Describe the morphology of the erythrocytes.
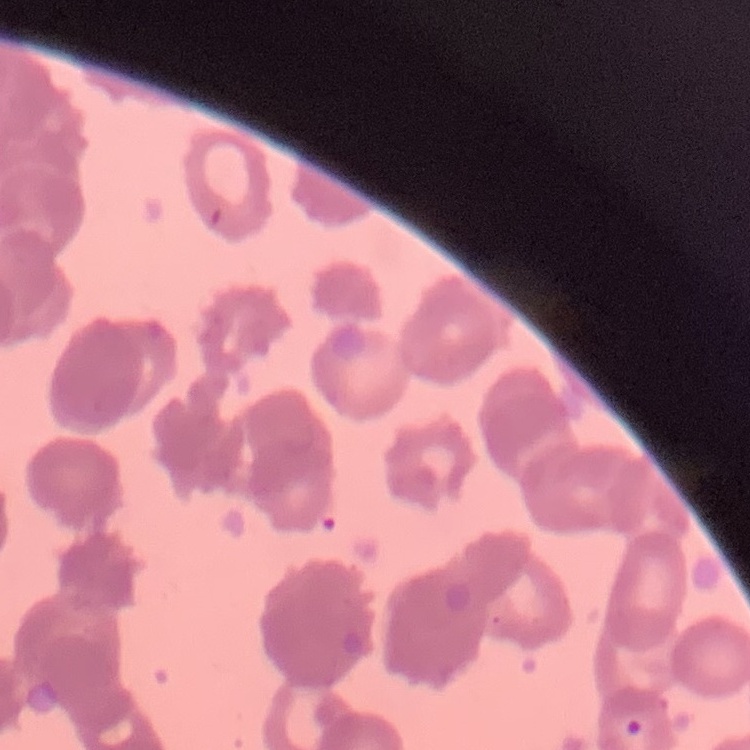

They show rouleaux formation.

image_type: one tile cut from a larger photomicrograph
stain: Field's or Giemsa
preparation: thin blood film